Assess the morphology of the red blood cells.
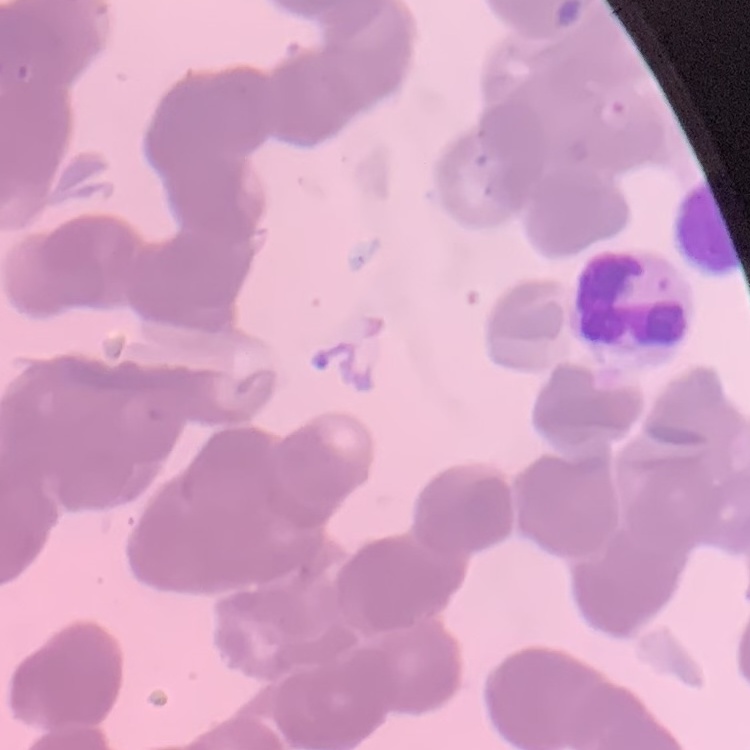

Rouleaux formation.

Summary:
  - Image type: square crop of a larger photomicrograph
  - Preparation: thin blood film
  - Stain: Field's or Giemsa